Draw a bounding box around every Plasmodium parasite.
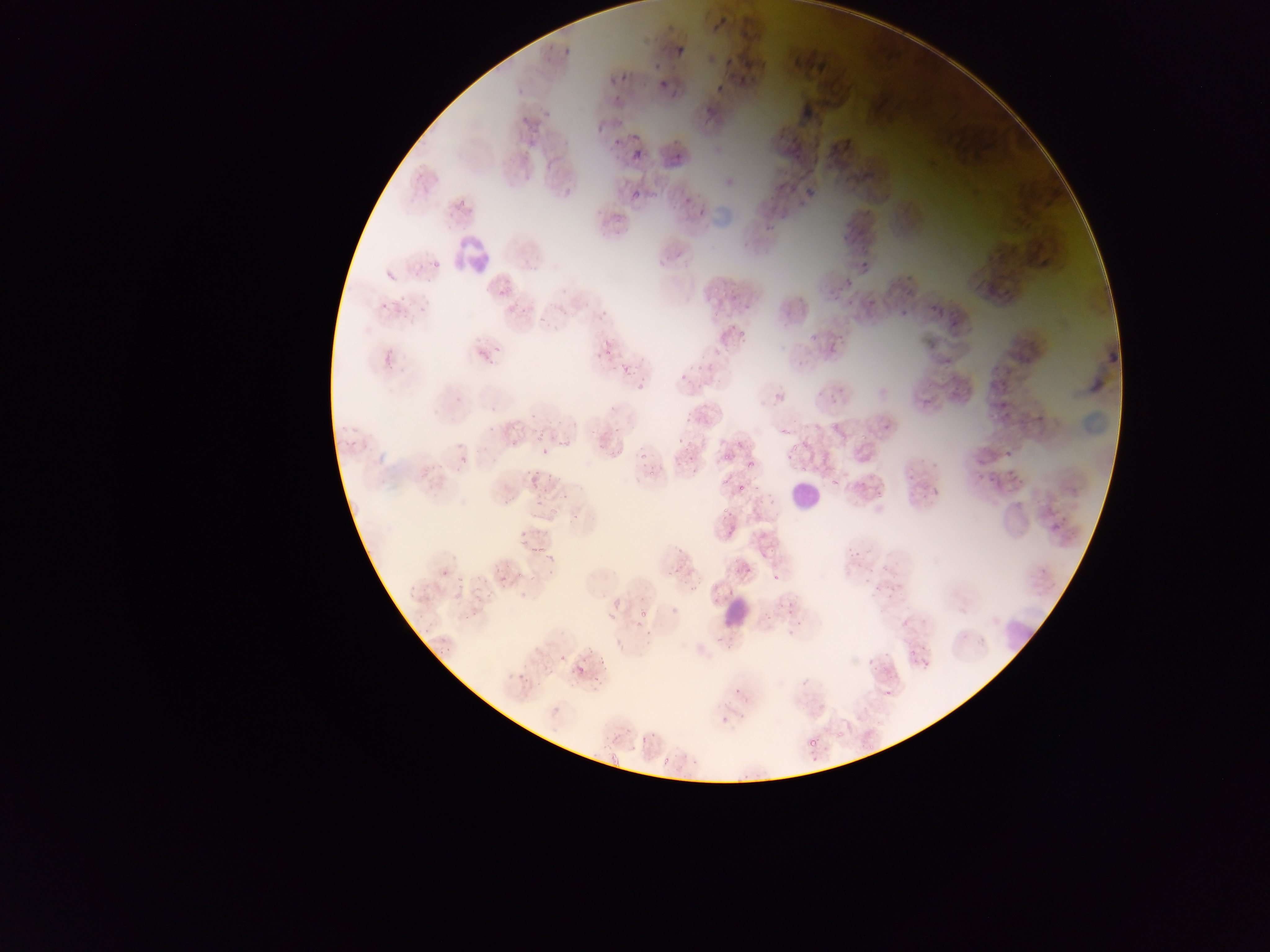
Approximate bounding boxes as {left, top, right, bottom} in pixels.
Plasmodium parasites: {621, 71, 627, 83}, {611, 73, 616, 85}, {658, 83, 669, 88}, {716, 85, 724, 94}, {598, 122, 603, 132}, {634, 147, 642, 155}, {807, 187, 815, 198}, {631, 190, 644, 201}, {432, 260, 439, 268}, {498, 291, 506, 296}, {833, 292, 841, 300}, {493, 344, 501, 353}, {861, 433, 869, 439}, {537, 435, 541, 443}, {791, 443, 799, 451}, {639, 451, 647, 462}, {724, 452, 732, 460}, {747, 462, 754, 470}, {801, 466, 809, 474}, {738, 483, 743, 491}, {519, 540, 529, 545}, {539, 544, 544, 553}, {640, 607, 646, 619}, {606, 608, 614, 620}, {559, 648, 570, 662}, {599, 656, 606, 664}, {576, 666, 587, 677}, {593, 678, 603, 685}, {809, 733, 815, 750}, {663, 756, 669, 764} | approximate {x, y} pixel centers of objects too small to bound: {635, 137}, {678, 156}, {864, 264}, {850, 303}, {384, 305}, {608, 352}, {559, 443}, {788, 457}, {652, 471}, {725, 481}, {725, 509}, {775, 576}, {840, 734}.

Summary:
  - Leukocyte locations: {452, 238, 487, 272}, {791, 479, 813, 511}, {719, 590, 753, 629}, {1000, 616, 1034, 651}
  - Artifact (stain precipitate or debris) locations: {711, 202, 734, 232}, {1080, 404, 1110, 441}
  - Image size: 1270×952 pixels
  - Preparation: thin blood film
  - Capture: mobile-phone photograph through a microscope
  - Field of view: single
  - Country: Ghana